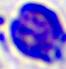
Summary:
  - Modality: micrograph
  - Magnification: 400x
  - Identification: white blood cell